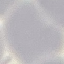
Malaria status: uninfected. Giemsa-stained preparation. Photographed with a smartphone camera at the microscope eyepiece. Automatically extracted cell patch, resized to 64 × 64 pixels. Thin smear of blood.